Assess the morphology of the erythrocytes.
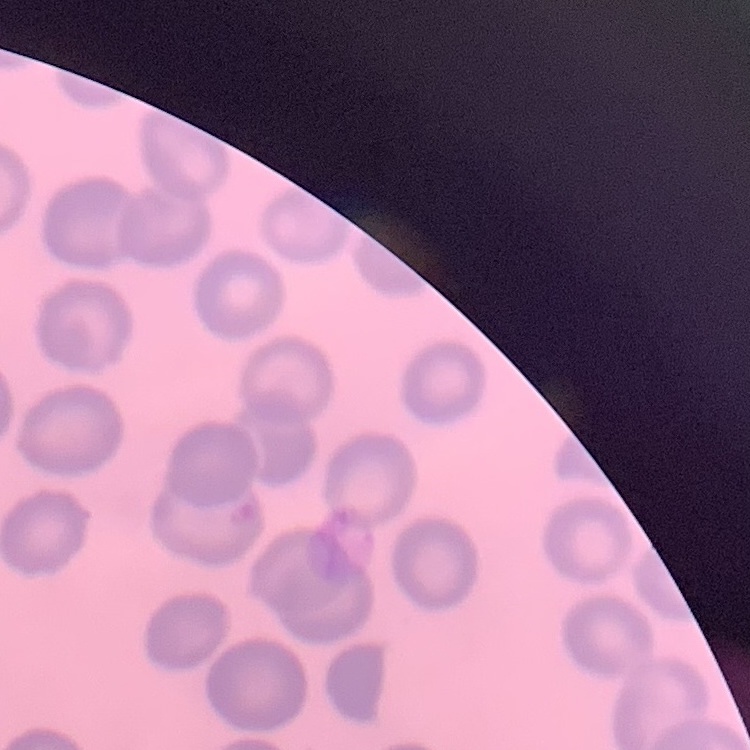

They show no rouleaux formation.

Summary:
  - Preparation: thin peripheral smear
  - Image type: square crop of a larger photomicrograph
  - Stain: Field's or Giemsa